Identify the parasite.
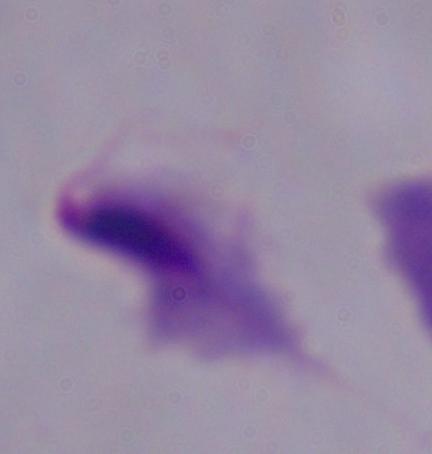

A trichomonad.

Summary:
  - Modality: micrograph
  - Magnification: 1000x